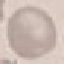

Malaria status: uninfected. Thin smear of blood. Giemsa-stained preparation. Cell patch, automatically extracted from a larger field of view and resized to 64 × 64 pixels. Photographed with a smartphone camera at the microscope eyepiece.